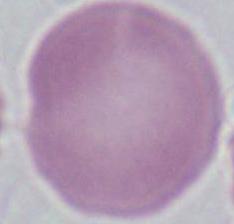 Photomicrograph. An erythrocyte is shown. 1000x magnification.